Locate every blood parasite and identify its species.
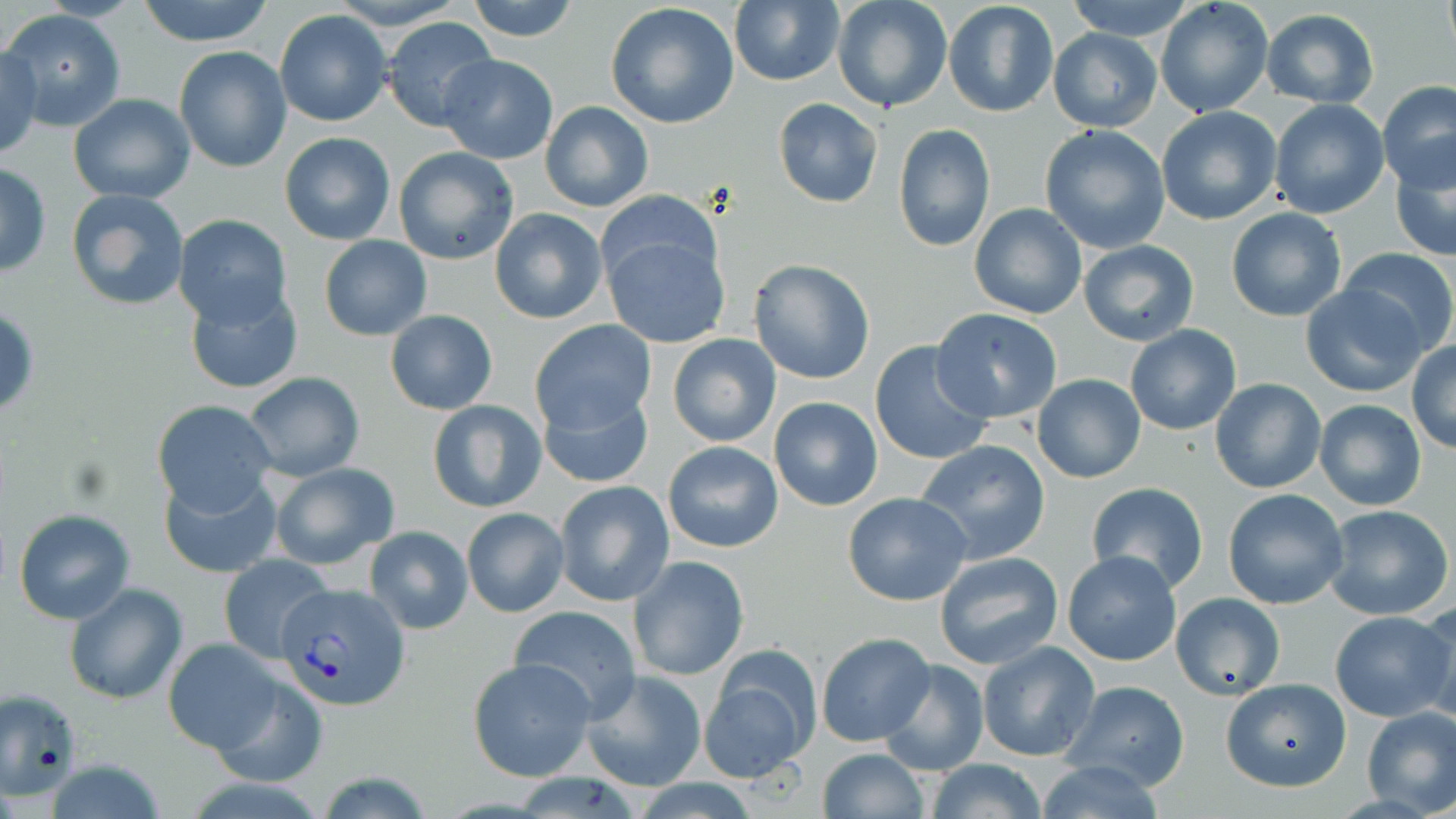
Approximate bounding boxes as named x1/y1/x2/y2 corners in pixels.
Plasmodium vivax-infected red blood cells: (x1=281, y1=583, x2=411, y2=711).
No Plasmodium falciparum, Plasmodium ovale, Plasmodium malariae, Babesia divergens, or Trypanosoma brucei observed.

{
  "slide_level_diagnosis": "Plasmodium vivax",
  "image_size": "1456×819 pixels",
  "uninfected_red_blood_cell_locations": "approximate bounding boxes as named x1/y1/x2/y2 corners in pixels: (x1=332, y1=0, x2=463, y2=28), (x1=464, y1=0, x2=581, y2=43), (x1=943, y1=0, x2=1059, y2=119), (x1=1063, y1=0, x2=1198, y2=39), (x1=1155, y1=0, x2=1273, y2=119), (x1=1440, y1=0, x2=1454, y2=57), (x1=133, y1=1, x2=278, y2=46), (x1=605, y1=2, x2=741, y2=129), (x1=728, y1=2, x2=844, y2=86), (x1=836, y1=3, x2=950, y2=113), (x1=1, y1=9, x2=126, y2=132), (x1=274, y1=10, x2=392, y2=127), (x1=1261, y1=10, x2=1380, y2=107), (x1=382, y1=16, x2=500, y2=134), (x1=1047, y1=29, x2=1162, y2=131), (x1=174, y1=45, x2=292, y2=173), (x1=0, y1=47, x2=43, y2=161), (x1=435, y1=54, x2=558, y2=163), (x1=1378, y1=81, x2=1456, y2=191), (x1=68, y1=93, x2=195, y2=204), (x1=772, y1=98, x2=882, y2=208), (x1=1270, y1=99, x2=1389, y2=219), (x1=541, y1=101, x2=652, y2=212), (x1=1156, y1=106, x2=1283, y2=225), (x1=893, y1=123, x2=995, y2=252), (x1=1039, y1=125, x2=1171, y2=254), (x1=280, y1=132, x2=395, y2=244), (x1=1389, y1=142, x2=1455, y2=264), (x1=394, y1=146, x2=519, y2=264), (x1=0, y1=161, x2=51, y2=276), (x1=67, y1=188, x2=189, y2=311), (x1=593, y1=191, x2=726, y2=306), (x1=969, y1=204, x2=1087, y2=319), (x1=1225, y1=207, x2=1347, y2=321), (x1=490, y1=209, x2=608, y2=324), (x1=173, y1=214, x2=293, y2=330), (x1=601, y1=231, x2=731, y2=351), (x1=319, y1=235, x2=432, y2=341), (x1=1078, y1=238, x2=1199, y2=346), (x1=1338, y1=247, x2=1456, y2=355), (x1=747, y1=259, x2=876, y2=385), (x1=183, y1=282, x2=304, y2=394), (x1=1300, y1=282, x2=1427, y2=397), (x1=931, y1=309, x2=1062, y2=424), (x1=385, y1=310, x2=497, y2=415), (x1=529, y1=319, x2=657, y2=437), (x1=1124, y1=324, x2=1243, y2=435), (x1=667, y1=333, x2=781, y2=448), (x1=870, y1=339, x2=995, y2=467), (x1=1406, y1=341, x2=1456, y2=454), (x1=1175, y1=345, x2=1304, y2=464), (x1=243, y1=372, x2=365, y2=481), (x1=1031, y1=374, x2=1146, y2=483), (x1=1210, y1=377, x2=1325, y2=493), (x1=536, y1=381, x2=654, y2=490), (x1=769, y1=396, x2=883, y2=511), (x1=427, y1=399, x2=547, y2=515), (x1=1314, y1=399, x2=1427, y2=512), (x1=152, y1=400, x2=277, y2=513), (x1=663, y1=439, x2=783, y2=553), (x1=915, y1=439, x2=1052, y2=565), (x1=268, y1=462, x2=400, y2=570), (x1=158, y1=469, x2=284, y2=580), (x1=553, y1=480, x2=675, y2=608), (x1=1086, y1=481, x2=1209, y2=593), (x1=1221, y1=489, x2=1349, y2=610), (x1=841, y1=493, x2=973, y2=607), (x1=1323, y1=504, x2=1455, y2=621), (x1=461, y1=507, x2=569, y2=617), (x1=13, y1=509, x2=135, y2=625), (x1=365, y1=525, x2=473, y2=635), (x1=1062, y1=550, x2=1183, y2=666), (x1=935, y1=551, x2=1064, y2=670), (x1=219, y1=555, x2=334, y2=663), (x1=628, y1=556, x2=749, y2=682), (x1=64, y1=582, x2=188, y2=705), (x1=1170, y1=593, x2=1284, y2=701), (x1=1415, y1=600, x2=1456, y2=723), (x1=509, y1=605, x2=642, y2=722), (x1=1329, y1=611, x2=1454, y2=722), (x1=816, y1=632, x2=936, y2=748), (x1=163, y1=638, x2=289, y2=756), (x1=977, y1=640, x2=1101, y2=761), (x1=702, y1=650, x2=820, y2=781), (x1=468, y1=658, x2=596, y2=781), (x1=878, y1=658, x2=989, y2=777), (x1=205, y1=669, x2=329, y2=787), (x1=578, y1=671, x2=708, y2=791), (x1=1220, y1=677, x2=1351, y2=791), (x1=1059, y1=680, x2=1189, y2=790), (x1=1, y1=688, x2=81, y2=798), (x1=1359, y1=705, x2=1455, y2=816), (x1=816, y1=748, x2=930, y2=819), (x1=925, y1=759, x2=1049, y2=819), (x1=1032, y1=759, x2=1168, y2=819)",
  "stain": "May-Grünwald-Giemsa",
  "modality": "light microscopy",
  "magnification": "1000x",
  "field_of_view": "one of a larger specimen",
  "preparation": "thin blood film"
}